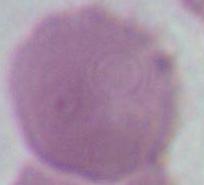
Summary:
  - Identification: red blood cell
  - Modality: micrograph
  - Magnification: 1000x